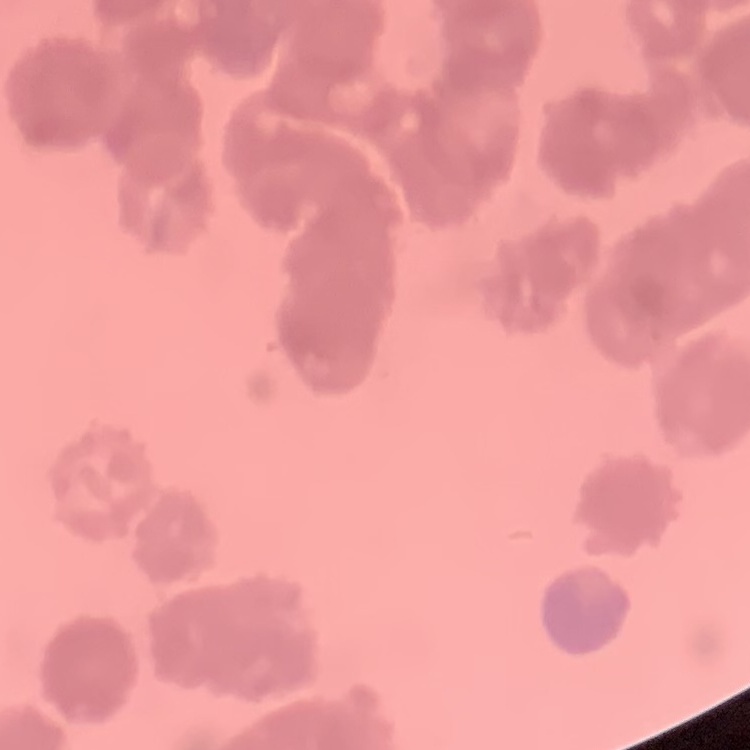
The red blood cells show rouleaux formation. Stained with either Field's or Giemsa. Thin blood smear. One tile cut from a larger photomicrograph.